State which parasite is depicted.
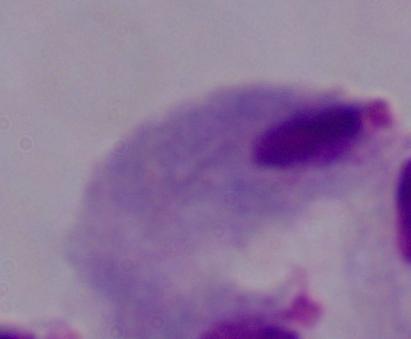
A trichomonad.

Summary:
  - Magnification: 1000x
  - Modality: photomicrograph